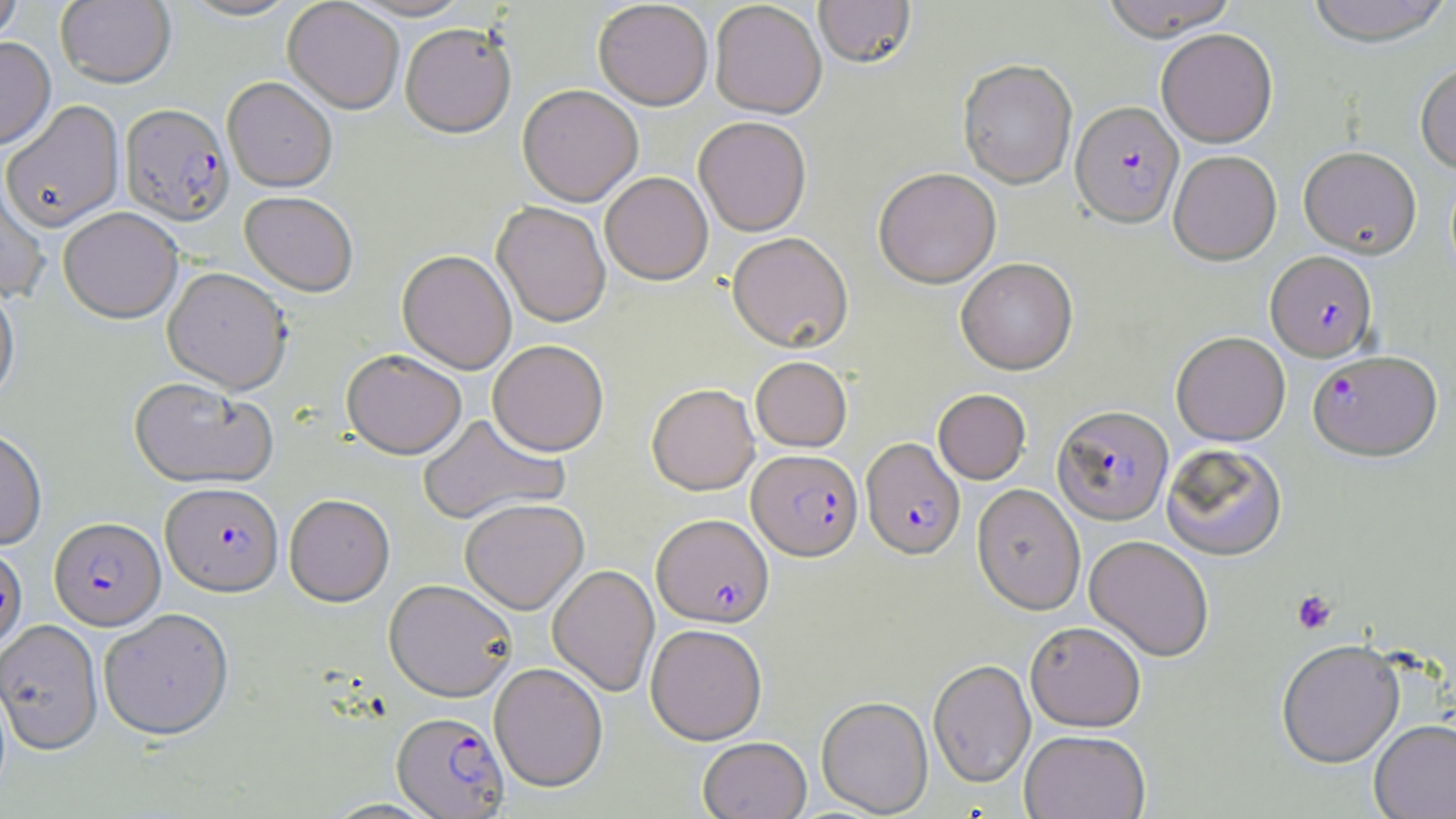 Approximate bounding boxes as (x1, y1, x2, y2) in pixels. Uninfected red blood cell locations: (56, 0, 176, 88), (179, 0, 301, 21), (282, 0, 404, 114), (347, 0, 473, 21), (814, 0, 916, 69), (1101, 0, 1238, 40), (1305, 0, 1454, 46), (0, 1, 23, 49), (593, 1, 713, 110), (710, 1, 826, 119), (285, 17, 518, 124), (400, 23, 516, 138), (1156, 28, 1277, 147), (0, 37, 56, 150), (958, 59, 1077, 188), (1415, 62, 1456, 173), (223, 76, 337, 191), (518, 85, 643, 206), (1, 101, 124, 231), (694, 116, 812, 236), (1298, 146, 1421, 258), (1168, 150, 1282, 265), (873, 167, 1001, 288), (600, 172, 713, 285), (0, 173, 51, 303), (240, 191, 358, 297), (492, 202, 611, 327), (58, 207, 183, 323), (727, 232, 853, 353), (397, 250, 517, 374), (955, 257, 1077, 374), (162, 266, 292, 393), (0, 279, 20, 409), (1172, 331, 1290, 445), (488, 339, 609, 456), (341, 349, 467, 459), (750, 356, 852, 451), (129, 378, 277, 489), (646, 383, 760, 495), (933, 388, 1031, 484), (418, 413, 569, 525), (0, 427, 47, 550), (1161, 442, 1288, 560), (972, 483, 1086, 615), (284, 494, 394, 607), (460, 499, 588, 614), (1084, 534, 1214, 661), (547, 564, 660, 697), (384, 579, 517, 702), (99, 608, 234, 741), (0, 619, 103, 755), (1025, 621, 1146, 731), (646, 623, 767, 744), (1276, 639, 1404, 767), (928, 658, 1036, 787), (490, 662, 608, 792), (817, 695, 932, 816), (1369, 718, 1456, 819), (1020, 729, 1150, 819), (698, 736, 811, 819). Platelet locations: (1291, 589, 1337, 634). Plasmodium falciparum-infected red blood cell locations: (1071, 100, 1183, 227), (120, 103, 234, 226), (1266, 250, 1377, 361), (1308, 349, 1442, 460), (1053, 404, 1173, 525), (861, 437, 966, 559), (747, 449, 863, 561), (162, 482, 284, 596), (652, 513, 773, 628), (49, 517, 165, 630), (0, 543, 27, 653), (392, 712, 509, 818). Slide-level diagnosis: Plasmodium falciparum. Image is 1456×819 pixels. Thin blood film. May-Grünwald-Giemsa stain. Captured at 1000x magnification. Single field of view. Light microscopy.